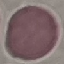
Malaria status: uninfected. Giemsa-stained preparation. Cell patch, automatically extracted from a larger field of view and resized to 64 × 64 pixels. Photographed with a smartphone camera at the microscope eyepiece. Thin smear of blood.